Name the parasite shown.
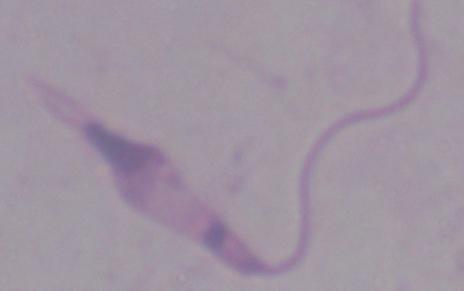
This is Leishmania.

1000x magnification. Photomicrograph.